Point out each Plasmodium parasite.
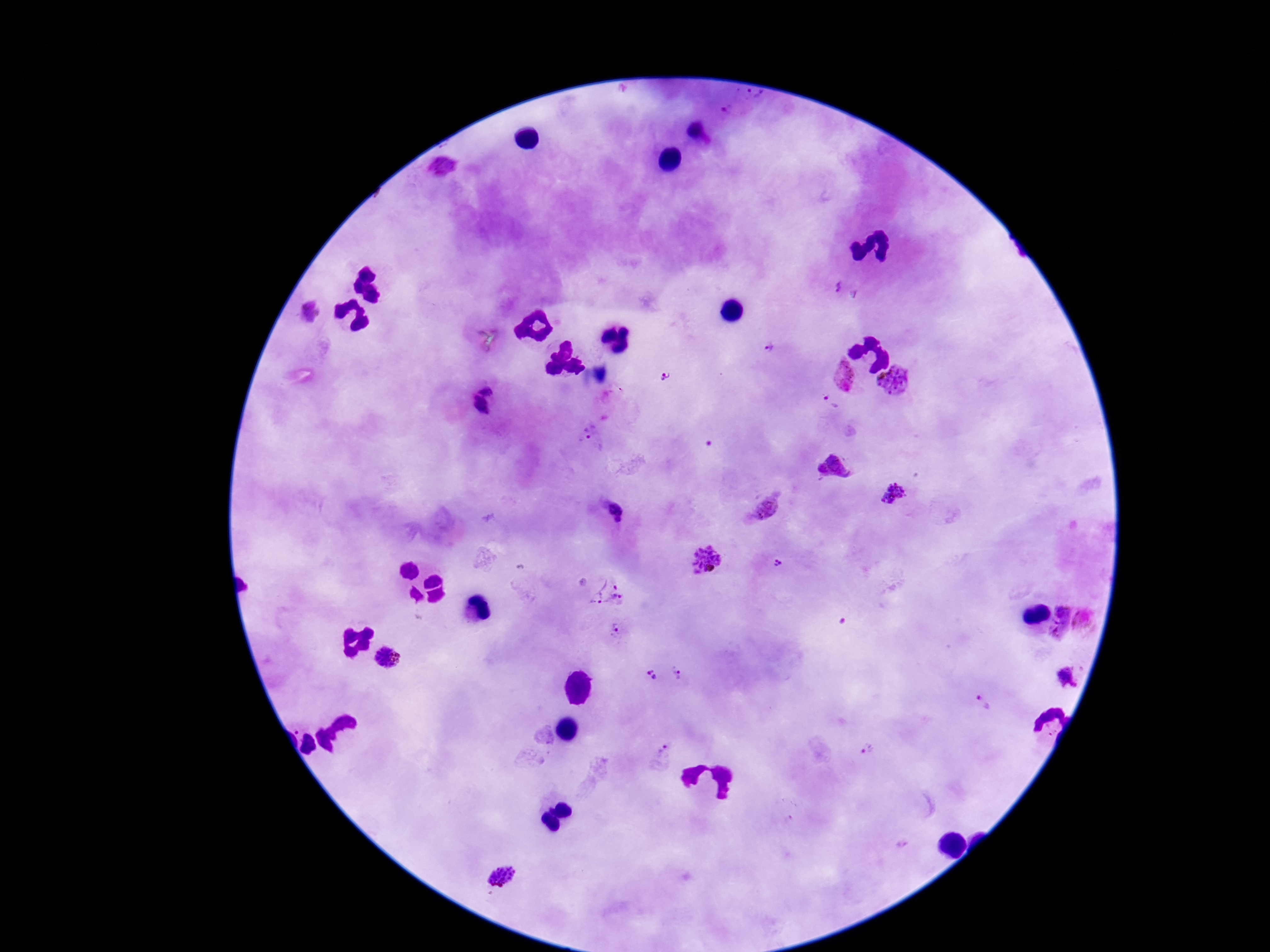
Approximate centers as (x, y) in pixels.
Plasmodium parasites: (756, 94), (731, 109), (695, 135), (444, 167), (836, 288), (311, 313), (769, 348), (666, 377), (845, 377), (896, 381), (486, 387), (829, 404), (479, 407), (590, 434), (894, 495), (764, 509), (705, 560), (777, 563), (609, 592), (1085, 622), (1062, 623), (618, 631), (388, 659), (678, 675), (650, 678), (1067, 678), (984, 702), (867, 750), (663, 754), (903, 845), (502, 875).

preparation = thick blood film
magnification = 100x
stain = Giemsa
patient malaria status = infected
field of view = single
image size = 1270×952 pixels
capture = smartphone camera through the microscope eyepiece